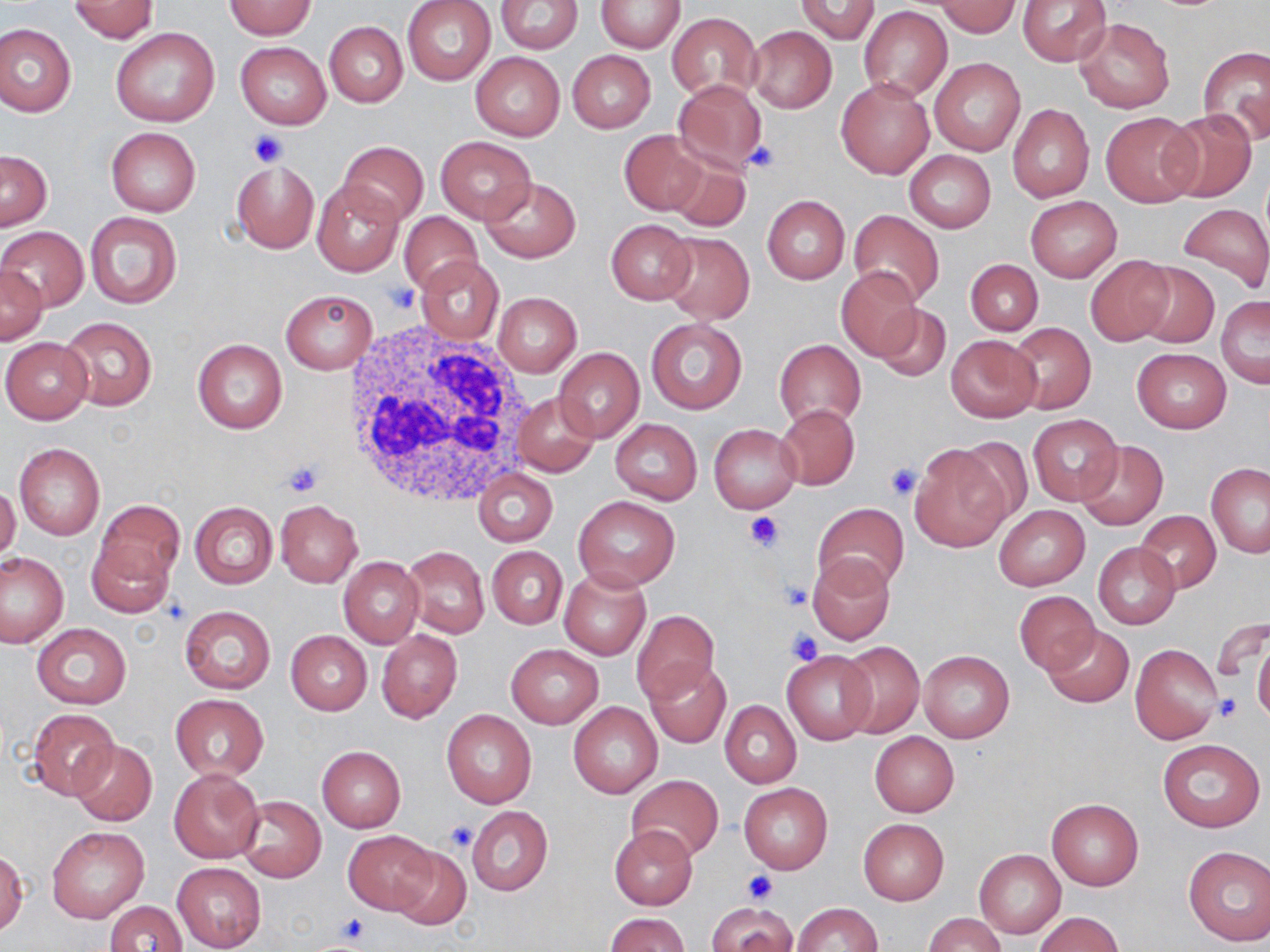

slide-level diagnosis = no evidence of blood parasites
field of view = one of a larger specimen
preparation = thin blood smear
uninfected red blood cell locations = approximate bounding boxes as [x1, y1, x2, y2] in pixels: [403, 0, 495, 85], [495, 0, 583, 53], [1017, 0, 1112, 67], [69, 1, 160, 42], [598, 1, 684, 52], [793, 1, 881, 44], [225, 2, 316, 38], [934, 2, 1023, 36], [860, 6, 952, 100], [667, 12, 761, 103], [1074, 16, 1174, 113], [324, 21, 408, 106], [0, 23, 76, 116], [748, 25, 836, 114], [109, 26, 221, 126], [236, 42, 330, 129], [1198, 46, 1270, 148], [566, 50, 654, 133], [470, 52, 566, 142], [929, 57, 1026, 158], [836, 78, 934, 179], [672, 79, 769, 174], [1008, 104, 1093, 201], [1162, 110, 1257, 203], [1099, 111, 1200, 206], [106, 127, 200, 216], [620, 131, 707, 215], [434, 136, 536, 224], [337, 140, 429, 226], [664, 148, 753, 232], [1, 150, 53, 230], [904, 151, 996, 232], [231, 159, 319, 253], [479, 176, 581, 263], [311, 178, 403, 277], [762, 195, 850, 284], [1025, 197, 1121, 281], [1176, 203, 1270, 295], [84, 211, 182, 310], [399, 211, 482, 294], [847, 211, 946, 306], [606, 219, 697, 305], [0, 226, 89, 312], [658, 231, 755, 324], [1084, 254, 1176, 346], [417, 257, 503, 343], [965, 259, 1043, 335], [1133, 262, 1218, 348], [1, 265, 47, 343], [836, 269, 925, 361], [280, 289, 378, 374], [494, 293, 581, 376], [1215, 295, 1269, 388], [870, 304, 950, 383], [59, 316, 157, 411], [646, 317, 747, 414], [1007, 323, 1095, 414], [945, 335, 1040, 421], [1, 337, 93, 423], [193, 338, 287, 433], [774, 339, 866, 429], [553, 347, 644, 442], [1131, 347, 1232, 433], [514, 390, 600, 476], [776, 404, 860, 489], [1028, 414, 1122, 505], [610, 418, 702, 504], [709, 424, 801, 513], [949, 436, 1036, 526], [1074, 439, 1169, 531], [14, 442, 105, 540], [910, 445, 1009, 551], [1206, 463, 1270, 558], [472, 468, 557, 546], [1147, 479, 1266, 588], [0, 484, 21, 564], [573, 496, 680, 590], [92, 500, 182, 597], [275, 500, 362, 587], [189, 501, 277, 590], [812, 502, 910, 598], [994, 505, 1090, 590], [1135, 510, 1220, 593], [1093, 543, 1181, 629], [402, 545, 489, 638], [487, 546, 567, 630], [1, 552, 67, 647], [806, 553, 898, 646], [339, 557, 425, 647], [560, 569, 651, 660], [1013, 591, 1098, 676], [178, 605, 275, 694], [630, 610, 718, 704], [1240, 619, 1268, 715], [31, 623, 131, 708], [1041, 624, 1133, 708], [376, 629, 462, 723], [285, 630, 372, 714], [1253, 638, 1270, 728], [835, 640, 924, 739], [1130, 643, 1224, 745], [505, 644, 603, 729], [782, 649, 876, 744], [918, 650, 1014, 742], [643, 658, 730, 747], [170, 693, 269, 782], [721, 701, 801, 788], [568, 702, 662, 798], [26, 707, 120, 800], [441, 710, 536, 808], [870, 731, 959, 817], [1157, 739, 1265, 832], [70, 741, 156, 826], [317, 746, 405, 832], [168, 766, 265, 863], [625, 774, 723, 863], [739, 782, 833, 873], [237, 796, 326, 882], [1046, 798, 1144, 891], [466, 806, 553, 897], [858, 819, 949, 904], [47, 826, 149, 923], [609, 826, 698, 909], [344, 830, 438, 913], [388, 844, 471, 929], [1183, 845, 1270, 945], [974, 848, 1065, 938], [1, 850, 27, 936], [172, 863, 266, 951], [104, 900, 187, 952], [706, 902, 800, 952], [792, 902, 881, 952], [1034, 912, 1123, 952], [606, 913, 689, 952], [925, 913, 1005, 952]
white blood cell locations = approximate bounding boxes as [x1, y1, x2, y2] in pixels: [341, 322, 537, 508]
platelet locations = approximate bounding boxes as [x1, y1, x2, y2] in pixels: [245, 128, 289, 168], [742, 140, 783, 176], [385, 283, 418, 314], [280, 458, 325, 498], [883, 460, 923, 500], [744, 512, 784, 554], [779, 581, 814, 610], [786, 628, 825, 666], [1212, 695, 1242, 722], [445, 821, 480, 852], [742, 868, 777, 903], [335, 914, 370, 945]
image size = 1270×952 pixels
modality = light microscopy
magnification = 1000x
stain = May-Grünwald-Giemsa